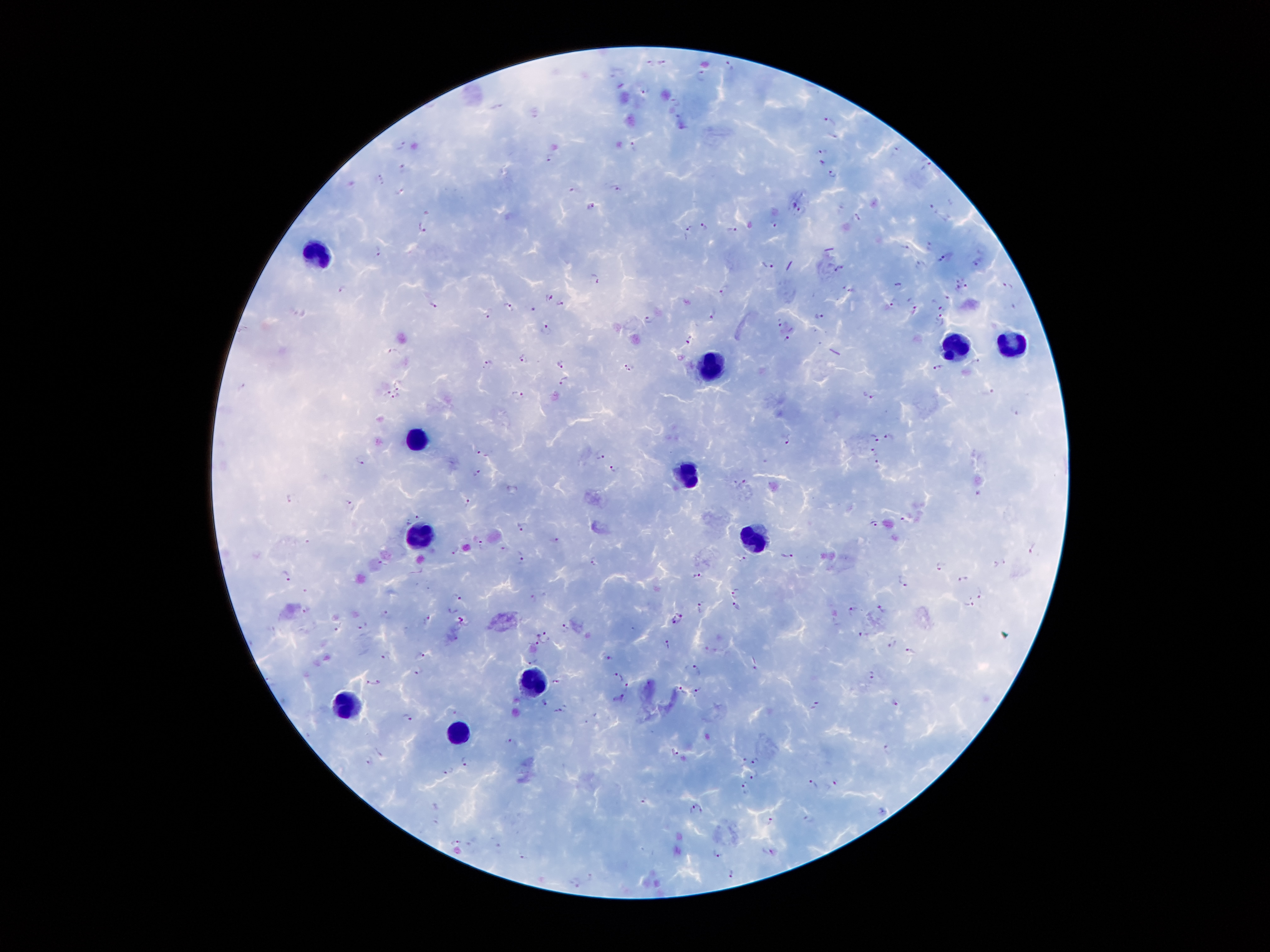 Approximate centers as (x, y) in pixels. Plasmodium parasite locations: (664, 61), (650, 62), (730, 65), (703, 75), (647, 90), (676, 103), (496, 106), (831, 121), (402, 144), (634, 146), (897, 149), (821, 151), (550, 158), (821, 161), (927, 163), (402, 168), (832, 173), (381, 178), (616, 186), (571, 188), (399, 191), (591, 205), (795, 206), (934, 209), (424, 210), (856, 214), (707, 224), (775, 224), (422, 227), (688, 229), (732, 229), (931, 243), (905, 245), (379, 250), (942, 256), (979, 262), (769, 264), (920, 266), (839, 268), (594, 277), (958, 281), (899, 282), (966, 285), (1008, 285), (342, 288), (851, 288), (959, 288), (723, 289), (549, 296), (949, 298), (894, 301), (560, 302), (433, 303), (508, 306), (915, 307), (942, 308), (533, 310), (303, 311), (491, 314), (713, 314), (939, 315), (818, 317), (648, 319), (782, 320), (545, 328), (788, 337), (688, 340), (396, 351), (525, 356), (976, 360), (562, 363), (489, 365), (630, 367), (938, 367), (565, 379), (399, 385), (244, 386), (987, 391), (385, 392), (871, 394), (518, 396), (397, 397), (1015, 410), (890, 436), (875, 437), (785, 439), (874, 451), (484, 452), (602, 456), (362, 459), (878, 465), (612, 469), (479, 471), (742, 483), (978, 491), (290, 497), (347, 500), (468, 501), (417, 516), (905, 518), (873, 522), (519, 524), (479, 539), (554, 539), (504, 548), (1033, 548), (454, 551), (786, 555), (521, 556), (742, 558), (594, 559), (1005, 561), (382, 563), (996, 564), (939, 566), (694, 574), (286, 575), (964, 578), (900, 579), (301, 589), (734, 591), (980, 593), (461, 596), (535, 596), (969, 604), (736, 605), (701, 606), (852, 609), (883, 609), (306, 611), (385, 614), (680, 615), (460, 620), (427, 621), (673, 623), (338, 625), (363, 625), (566, 626), (862, 633), (544, 635), (533, 642), (667, 644), (892, 645), (910, 650), (422, 652), (385, 654), (610, 657), (533, 661), (754, 665), (696, 667), (419, 672), (618, 675), (875, 676), (557, 679), (377, 680), (368, 681), (626, 683), (684, 689), (699, 689), (621, 698), (545, 702), (896, 703), (816, 705), (560, 710), (456, 712), (407, 715), (507, 740), (887, 746), (378, 751), (677, 751), (368, 758), (756, 759), (744, 761), (465, 762), (448, 770), (753, 774), (836, 781), (813, 782), (746, 783), (645, 800), (696, 807), (770, 820), (457, 841), (497, 841), (774, 851), (718, 853), (522, 857), (731, 874), (592, 875), (577, 883). Leukocyte locations: (314, 257), (1015, 338), (957, 346), (714, 370), (418, 439), (689, 472), (418, 536), (750, 539), (536, 679), (341, 705), (462, 733). Thick peripheral-blood smear. Giemsa stain. One field from this slide. Photographed through the microscope eyepiece with a smartphone camera. Patient malaria status: infected with Plasmodium falciparum. Image is 1270×952 pixels. 100x magnification.